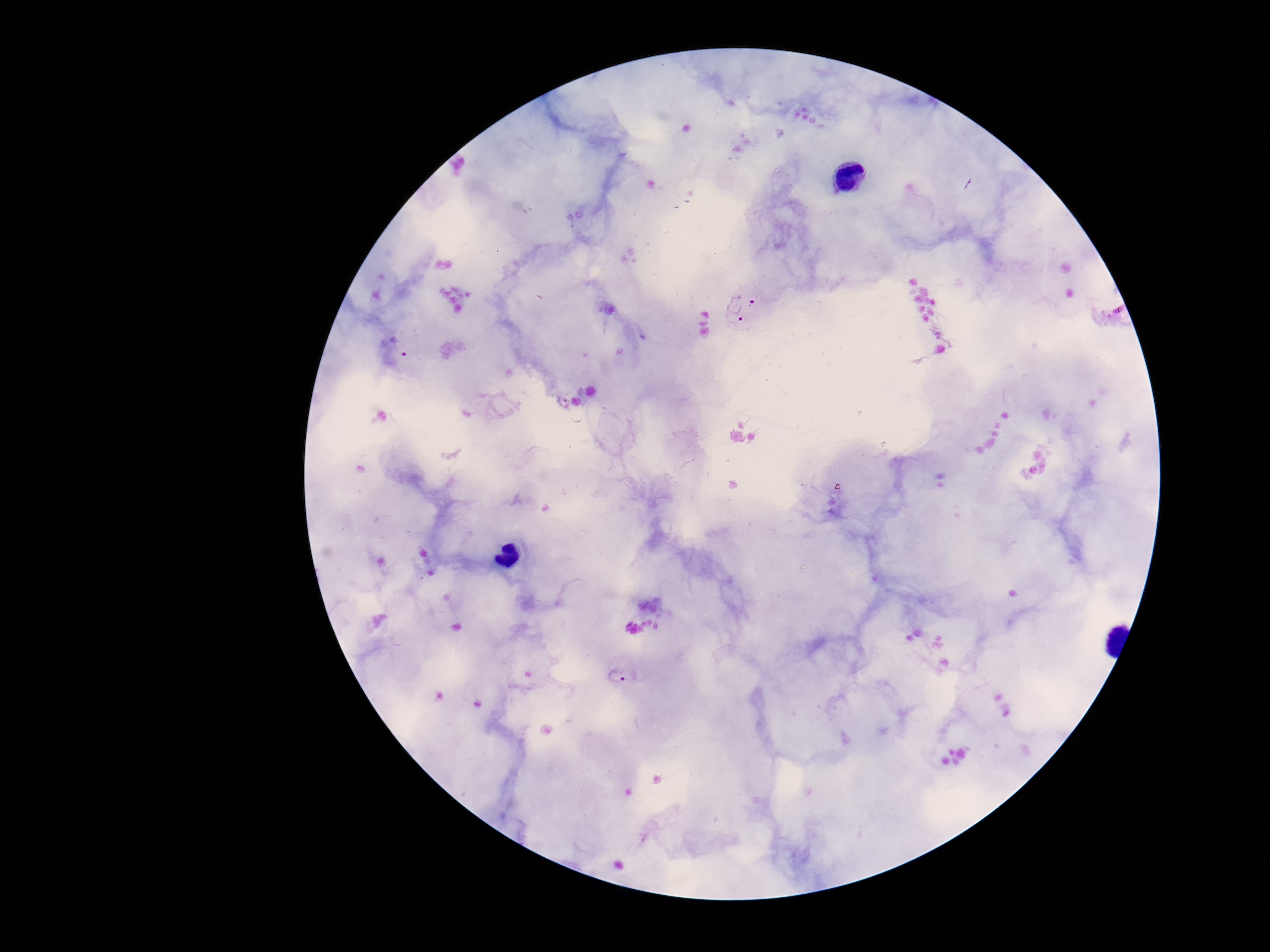 Approximate centers as {x, y} in pixels. Plasmodium parasite locations: {740, 307}, {619, 676}. One field from this slide. Patient malaria status: infected. Image is 1270×952 pixels. Giemsa-stained preparation. Smartphone photograph taken through the microscope eyepiece. 100x magnification. Thick blood film.